Locate every Plasmodium parasite.
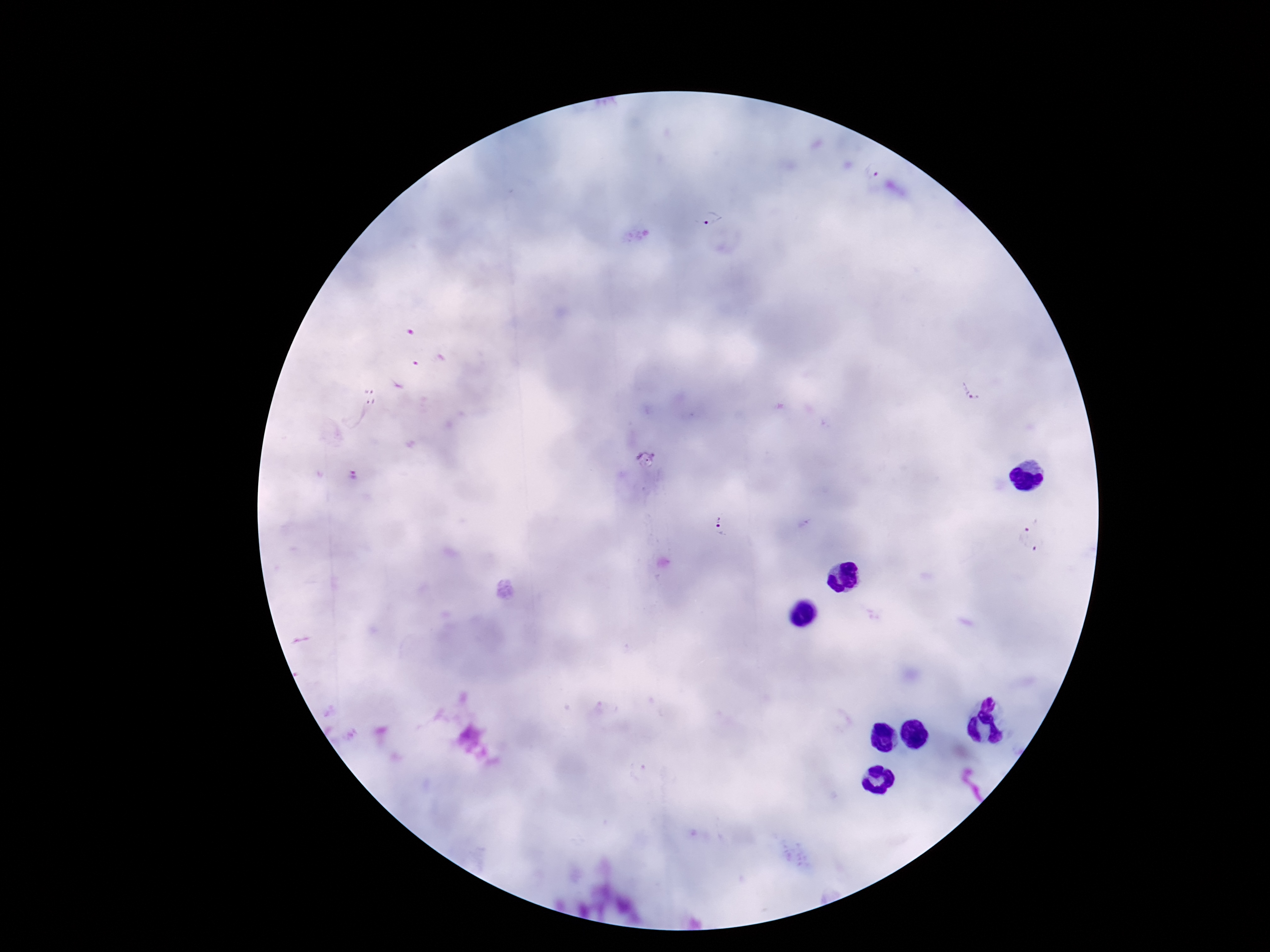
Approximate centers as (x, y) in pixels.
Plasmodium parasites: (870, 172), (711, 217), (973, 387), (370, 397), (721, 519), (1023, 531), (1041, 549).

Summary:
  - Image size: 1270×952 pixels
  - Field of view: single
  - Magnification: 100x
  - Preparation: thick blood smear
  - Capture: smartphone camera through the microscope eyepiece
  - Stain: Giemsa
  - Patient malaria status: infected